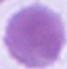

Summary:
  - Identification: red blood cell
  - Magnification: 1000x
  - Modality: photomicrograph